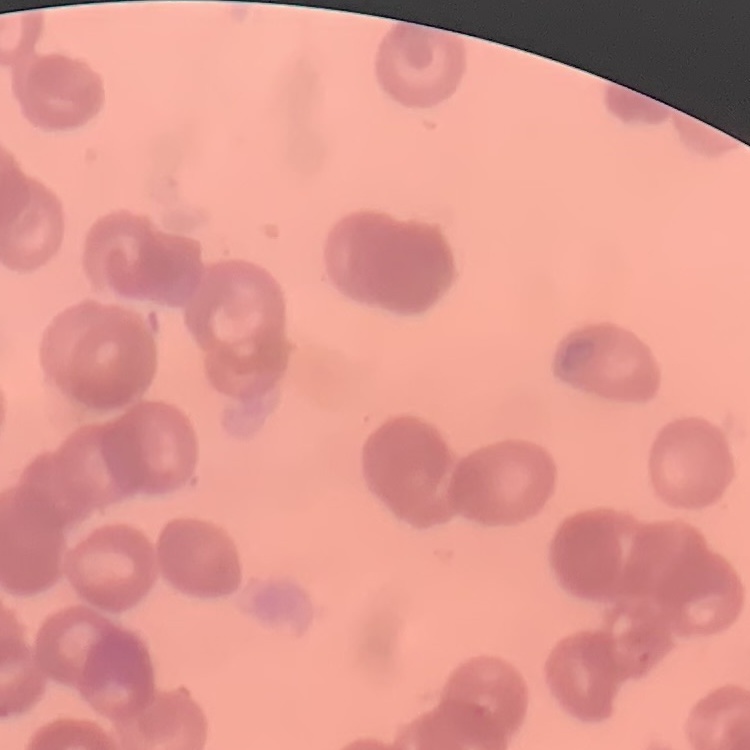

{
  "erythrocyte_morphology": "rouleaux formation",
  "preparation": "thin peripheral smear",
  "image_type": "square crop of a larger photomicrograph",
  "stain": "Field's or Giemsa"
}